Assess this cell for malaria.
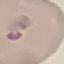
Uninfected.

Thin blood smear. Giemsa-stained preparation. Cell patch, automatically extracted from a larger field of view and resized to 64 × 64 pixels. Photographed with a smartphone camera at the microscope eyepiece.